Classify this cell by malaria status.
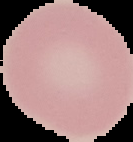
It is uninfected.

{
  "image_type": "segmented cell region with the area outside set to black",
  "preparation": "thin blood film",
  "image_size": "133×142 pixels"
}